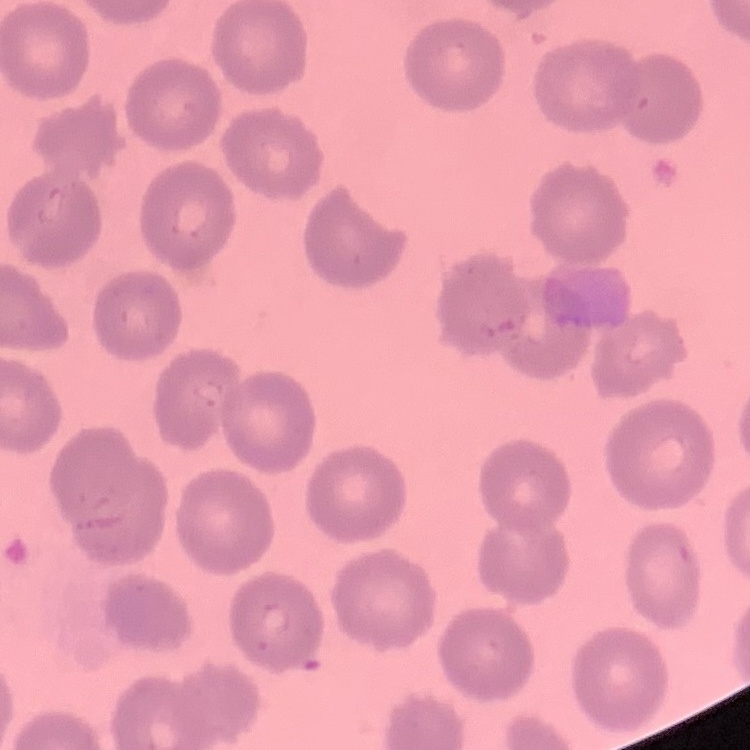

The red blood cells show no rouleaux formation. Thin peripheral smear. One tile cut from a larger photomicrograph. Field's or Giemsa stain.